State which cell type is depicted.
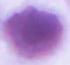

An erythrocyte.

Summary:
  - Modality: micrograph
  - Magnification: 1000x